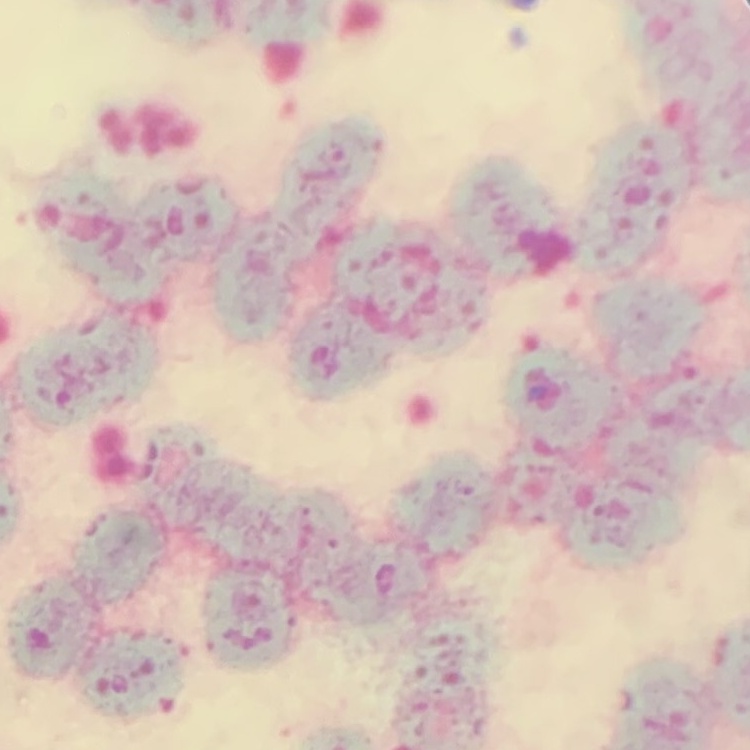
The erythrocytes show rouleaux formation. Thin blood smear. Field's or Giemsa stain. Square crop of a larger photomicrograph.